Locate every uninfected red blood cell.
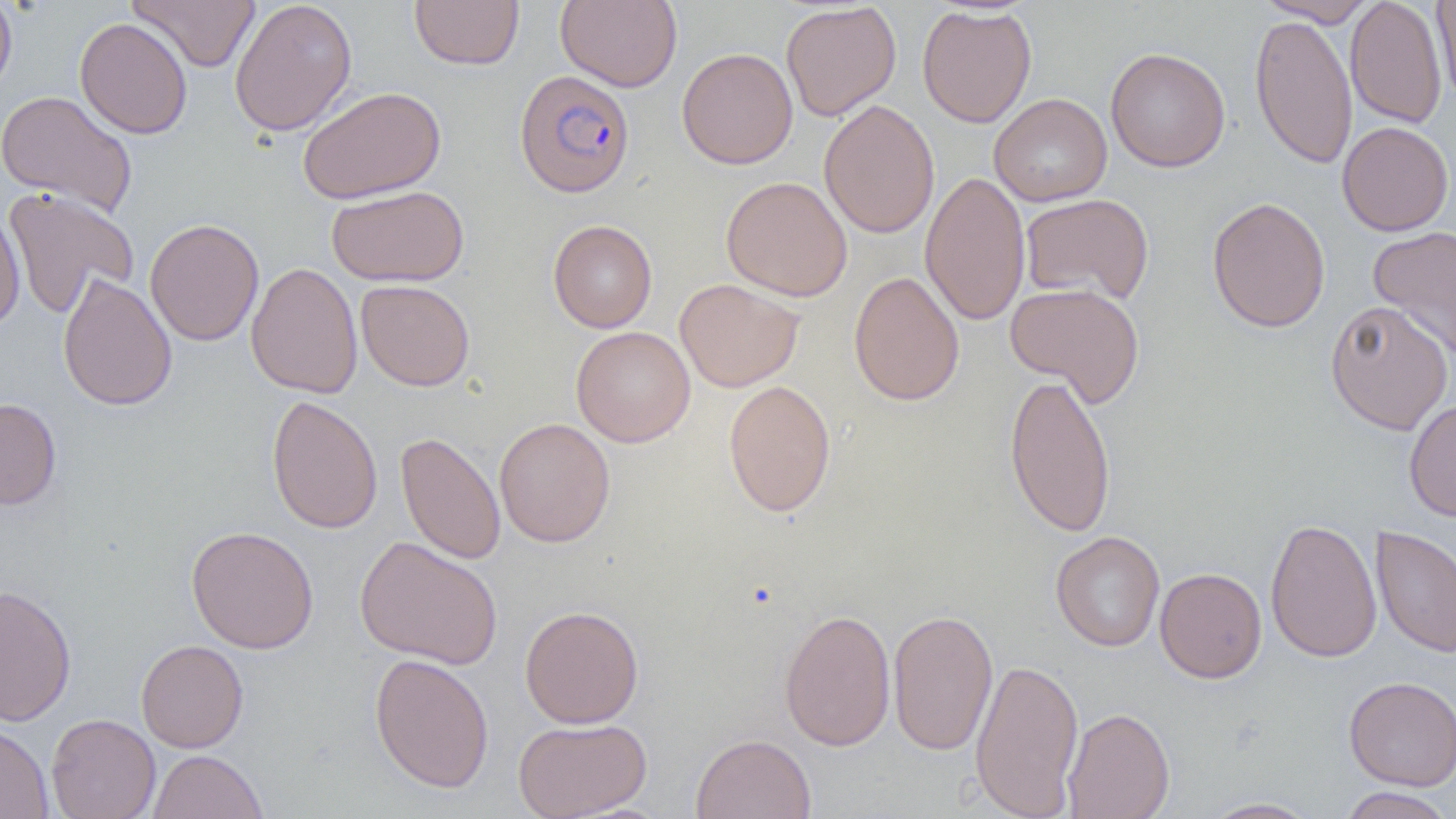
Approximate bounding boxes as named x1/y1/x2/y2 corners in pixels.
Uninfected red blood cells: (x1=0, y1=0, x2=18, y2=101), (x1=128, y1=0, x2=261, y2=71), (x1=229, y1=0, x2=357, y2=137), (x1=409, y1=0, x2=524, y2=70), (x1=555, y1=0, x2=682, y2=92), (x1=1256, y1=0, x2=1376, y2=26), (x1=1345, y1=0, x2=1447, y2=129), (x1=1431, y1=0, x2=1456, y2=105), (x1=780, y1=1, x2=901, y2=121), (x1=916, y1=5, x2=1037, y2=128), (x1=1249, y1=13, x2=1358, y2=170), (x1=75, y1=17, x2=192, y2=139), (x1=1105, y1=46, x2=1230, y2=173), (x1=677, y1=47, x2=798, y2=170), (x1=298, y1=86, x2=446, y2=203), (x1=0, y1=90, x2=138, y2=218), (x1=989, y1=93, x2=1112, y2=207), (x1=818, y1=99, x2=940, y2=239), (x1=1337, y1=121, x2=1454, y2=236), (x1=920, y1=171, x2=1030, y2=326), (x1=721, y1=176, x2=852, y2=302), (x1=326, y1=185, x2=469, y2=286), (x1=3, y1=186, x2=139, y2=319), (x1=1020, y1=194, x2=1154, y2=306), (x1=1206, y1=196, x2=1331, y2=333), (x1=0, y1=207, x2=25, y2=331), (x1=144, y1=218, x2=264, y2=346), (x1=548, y1=219, x2=657, y2=333), (x1=1367, y1=225, x2=1456, y2=360), (x1=245, y1=261, x2=363, y2=399), (x1=848, y1=271, x2=964, y2=407), (x1=57, y1=272, x2=177, y2=411), (x1=674, y1=278, x2=805, y2=392), (x1=355, y1=279, x2=475, y2=391), (x1=1005, y1=283, x2=1145, y2=406), (x1=1325, y1=300, x2=1453, y2=435), (x1=570, y1=326, x2=696, y2=447), (x1=1005, y1=372, x2=1117, y2=538), (x1=722, y1=379, x2=837, y2=517), (x1=266, y1=394, x2=383, y2=535), (x1=0, y1=398, x2=62, y2=510), (x1=1404, y1=398, x2=1456, y2=522), (x1=494, y1=417, x2=615, y2=547), (x1=395, y1=431, x2=506, y2=566), (x1=1264, y1=517, x2=1382, y2=663), (x1=186, y1=525, x2=319, y2=654), (x1=1370, y1=525, x2=1456, y2=659), (x1=1050, y1=531, x2=1165, y2=652), (x1=354, y1=535, x2=504, y2=670), (x1=1154, y1=567, x2=1267, y2=683), (x1=0, y1=584, x2=76, y2=726), (x1=520, y1=604, x2=644, y2=728), (x1=778, y1=607, x2=896, y2=752), (x1=887, y1=607, x2=998, y2=756), (x1=136, y1=639, x2=249, y2=753), (x1=369, y1=653, x2=494, y2=793), (x1=970, y1=657, x2=1084, y2=818), (x1=1343, y1=675, x2=1456, y2=791), (x1=1062, y1=706, x2=1175, y2=819), (x1=46, y1=713, x2=160, y2=819), (x1=512, y1=717, x2=651, y2=819), (x1=0, y1=720, x2=53, y2=818), (x1=691, y1=732, x2=816, y2=819), (x1=147, y1=749, x2=268, y2=819), (x1=1337, y1=787, x2=1454, y2=819), (x1=1201, y1=797, x2=1321, y2=818).

Summary:
  - Plasmodium falciparum-infected red blood cell locations: (x1=514, y1=70, x2=636, y2=198)
  - Slide-level diagnosis: Plasmodium falciparum
  - Preparation: thin blood smear
  - Image size: 1456×819 pixels
  - Magnification: 1000x
  - Field of view: one of a larger specimen
  - Modality: optical microscopy